State the blood parasite species.
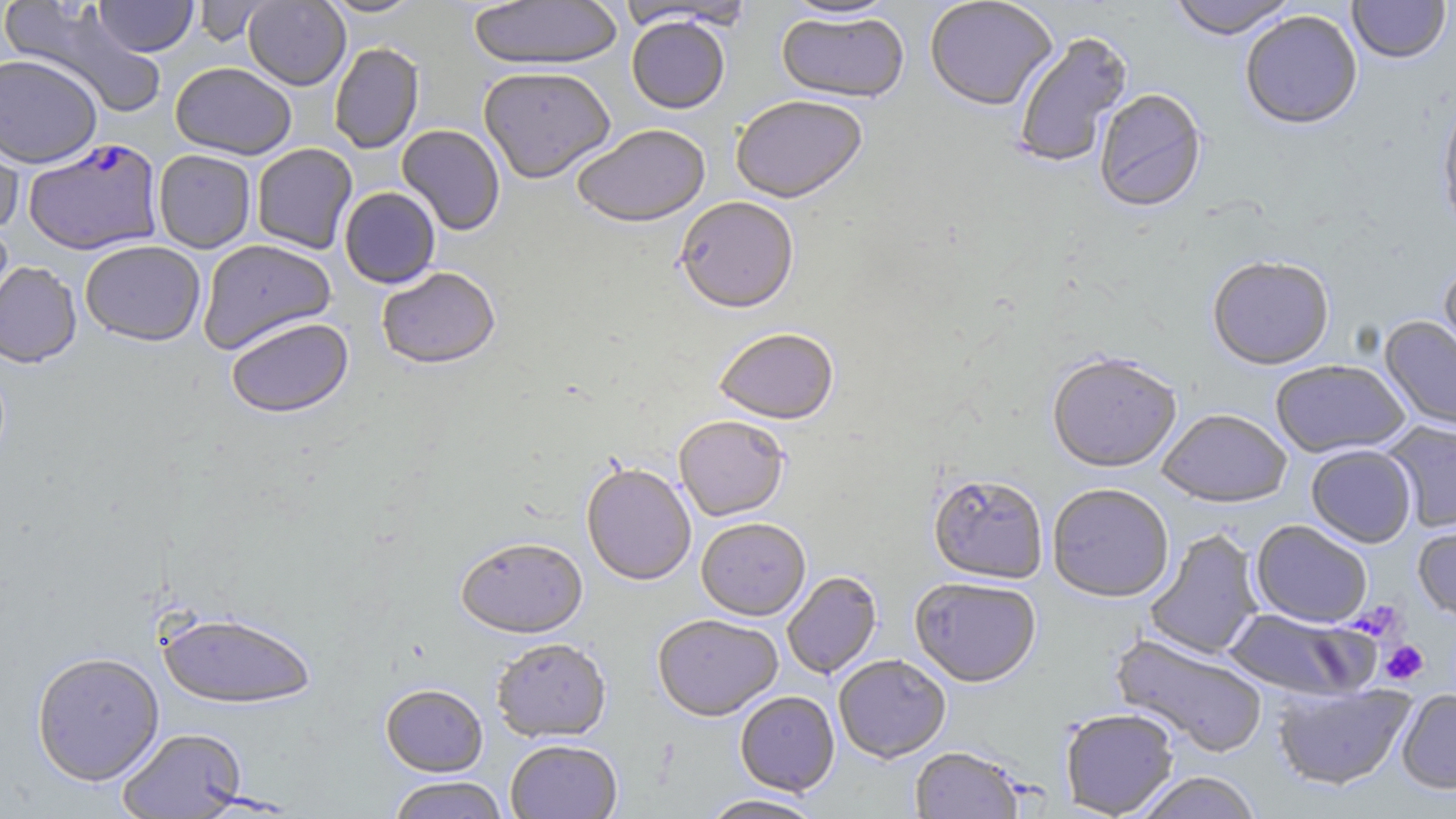
Plasmodium falciparum.

platelet locations = approximate bounding boxes as [x1, y1, x2, y2] in pixels: [1353, 600, 1407, 642], [1380, 640, 1428, 685]
preparation = thin blood film
image size = 1456×819 pixels
magnification = 1000x
modality = light microscopy
field of view = single
uninfected red blood cell locations = approximate bounding boxes as [x1, y1, x2, y2] in pixels: [93, 0, 198, 57], [243, 0, 350, 90], [319, 0, 425, 18], [468, 0, 623, 70], [924, 0, 1058, 110], [1167, 0, 1299, 39], [1347, 0, 1451, 64], [3, 1, 167, 118], [191, 1, 274, 47], [621, 1, 751, 31], [779, 1, 903, 21], [775, 9, 909, 103], [1240, 10, 1363, 129], [626, 15, 730, 113], [1011, 30, 1133, 169], [329, 42, 424, 153], [0, 53, 102, 168], [170, 62, 297, 159], [478, 64, 616, 183], [1094, 88, 1207, 213], [1437, 91, 1456, 234], [730, 94, 867, 203], [0, 117, 25, 237], [572, 123, 710, 227], [396, 124, 506, 235], [251, 143, 358, 254], [153, 149, 256, 253], [339, 187, 440, 288], [674, 196, 799, 313], [0, 221, 14, 332], [198, 239, 337, 353], [79, 240, 206, 346], [1207, 256, 1335, 369], [1438, 259, 1456, 376], [0, 260, 82, 367], [376, 266, 500, 369], [225, 315, 353, 417], [1379, 315, 1456, 435], [713, 326, 839, 424], [1047, 352, 1182, 472], [1270, 359, 1410, 457], [1157, 408, 1292, 507], [674, 414, 789, 521], [1383, 420, 1456, 533], [1306, 444, 1417, 547], [582, 462, 697, 585], [928, 472, 1048, 584], [1047, 482, 1174, 602], [696, 516, 810, 620], [1413, 517, 1456, 624], [1251, 520, 1373, 627], [1145, 529, 1264, 660], [455, 535, 588, 637], [781, 571, 883, 679], [909, 575, 1042, 687], [1223, 607, 1377, 701], [158, 609, 316, 708], [652, 613, 783, 720], [1110, 632, 1268, 758], [490, 637, 612, 742], [31, 650, 165, 785], [833, 654, 951, 762], [380, 682, 488, 776], [1272, 683, 1415, 791], [1397, 689, 1456, 794], [735, 691, 840, 796], [1060, 707, 1180, 818], [117, 726, 247, 817], [505, 739, 623, 818], [909, 746, 1026, 818], [1133, 771, 1263, 819], [387, 776, 510, 819], [698, 794, 826, 818]
stain = May-Grünwald-Giemsa
Plasmodium falciparum-infected red blood cell locations = approximate bounding boxes as [x1, y1, x2, y2] in pixels: [27, 139, 168, 256]